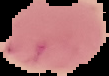 From a thin blood film. Segmented cell region on a black background. Image is 109×76 pixels. Result: negative for malaria parasites.